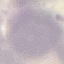
Result: no malaria parasites detected. Giemsa stain. Acquired by smartphone through the microscope eyepiece. Automatically extracted cell patch, resized to 64 × 64 pixels. Thin smear of blood.